Give the extent of all uninfected red blood cells.
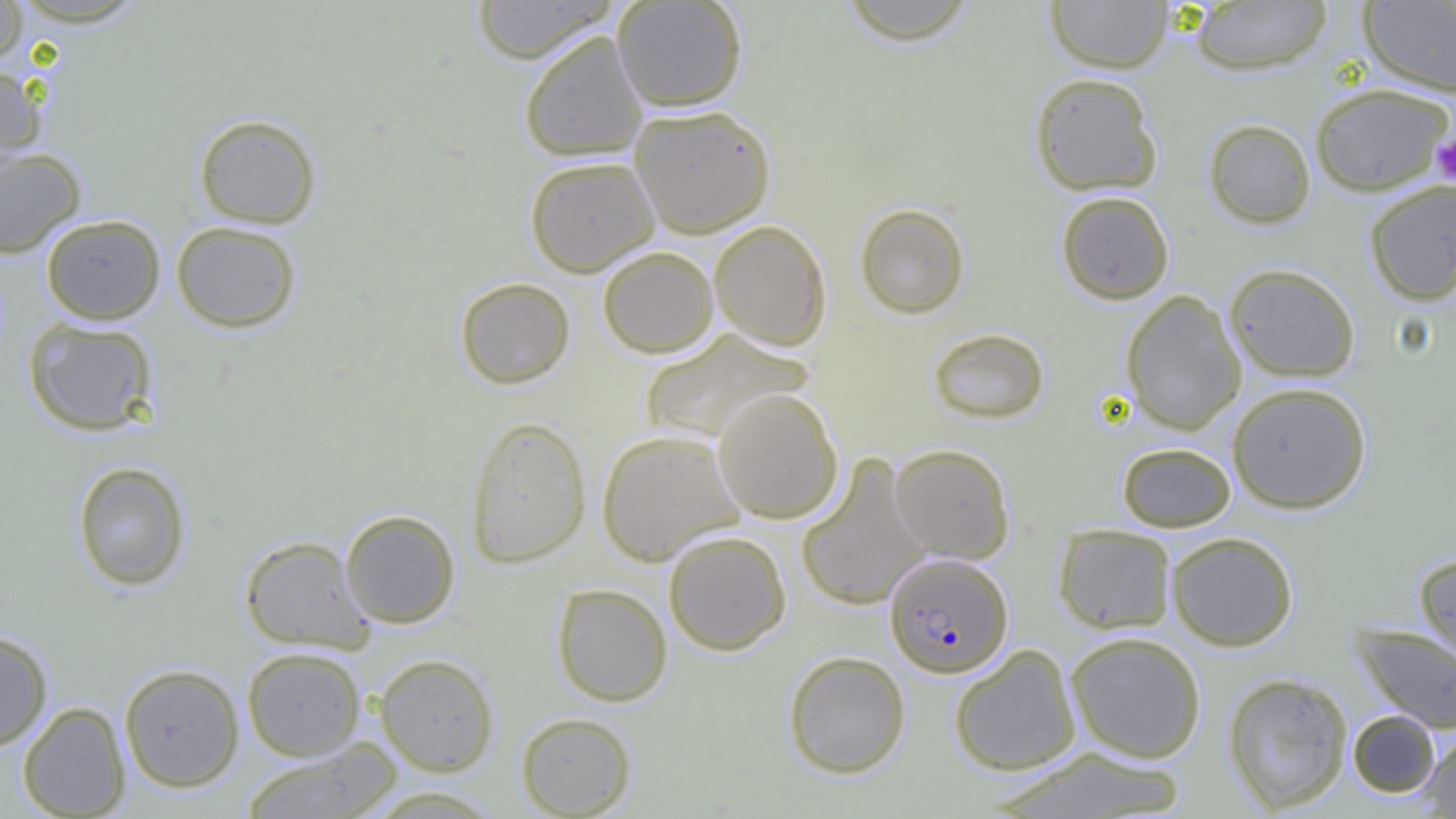
Approximate bounding boxes as (x1,y1)-(x2,y2) corner pairs in pixels.
Uninfected red blood cells: (0,0)-(28,66), (470,0)-(618,64), (612,0)-(747,111), (835,0)-(982,44), (1045,0)-(1173,73), (1187,1)-(1333,74), (1358,2)-(1456,97), (519,30)-(648,162), (0,62)-(47,173), (1029,72)-(1164,196), (1310,82)-(1453,196), (629,104)-(776,238), (194,113)-(322,228), (1203,118)-(1316,228), (0,146)-(86,258), (524,155)-(659,277), (1364,180)-(1456,305), (1056,191)-(1174,304), (854,203)-(970,319), (41,214)-(166,324), (709,220)-(832,351), (171,221)-(302,333), (597,246)-(719,358), (1224,263)-(1361,382), (455,276)-(575,389), (1120,290)-(1246,435), (23,316)-(159,436), (927,327)-(1050,424), (638,328)-(813,445), (1228,382)-(1371,513), (713,388)-(843,524), (465,415)-(592,568), (596,429)-(745,566), (1117,442)-(1235,531), (890,443)-(1016,563), (795,453)-(932,612), (71,461)-(191,591), (340,509)-(460,628), (1053,524)-(1177,635), (663,530)-(792,655), (1165,531)-(1299,651), (239,535)-(374,654), (1413,552)-(1456,669), (552,583)-(672,706), (1351,623)-(1456,735), (0,629)-(53,751), (1065,631)-(1207,763), (949,644)-(1081,776), (241,646)-(366,761), (783,650)-(911,778), (375,654)-(499,776), (119,663)-(245,793), (1221,671)-(1353,814), (17,701)-(131,818), (1347,710)-(1441,798), (516,711)-(637,817), (1421,731)-(1456,817), (242,738)-(401,819), (987,745)-(1192,818), (359,785)-(507,818).

Plasmodium falciparum-infected red blood cell locations: (885,552)-(1013,678). Platelet locations: (1431,134)-(1456,185). Slide-level diagnosis: Plasmodium falciparum. Thin blood film. Captured at 1000x magnification. One field of a larger specimen. Light microscopy. Image is 1456×819 pixels.